Give the position of every Plasmodium parasite visible.
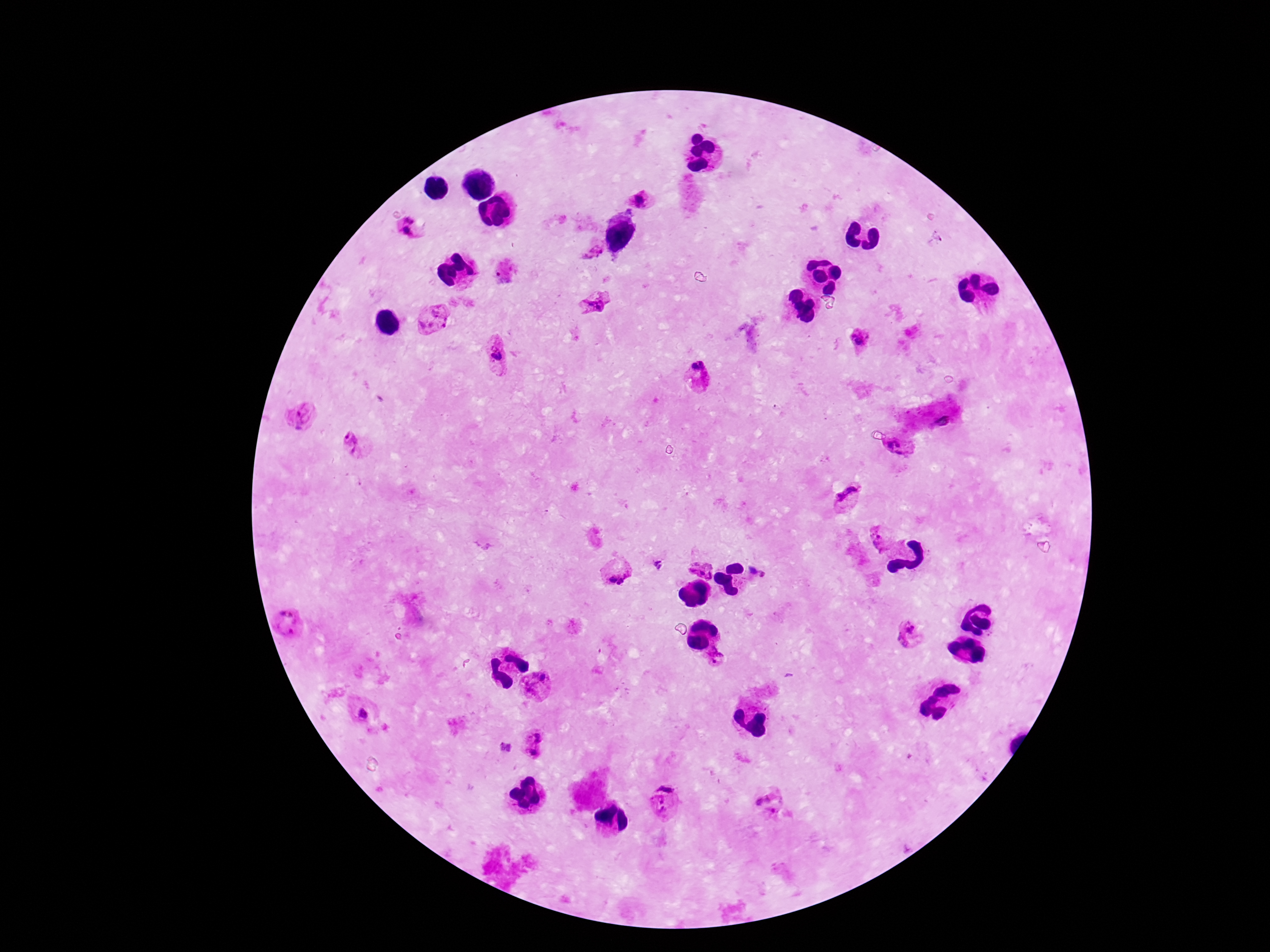
Approximate centers as (x, y) in pixels.
Plasmodium parasites: (642, 200), (406, 232), (594, 251), (506, 274), (596, 304), (434, 318), (861, 342), (498, 352), (700, 371), (304, 415), (943, 419), (353, 443), (900, 445), (846, 494), (881, 538), (656, 565), (699, 567), (760, 570), (616, 574), (286, 619), (912, 625), (903, 640), (721, 658), (539, 688), (365, 715), (538, 732), (531, 755), (661, 801), (769, 802).

image_size: 1270×952 pixels
patient_malaria_status: positive
capture: smartphone camera through the microscope eyepiece
stain: Giemsa
preparation: thick blood film
magnification: 100x
field_of_view: single